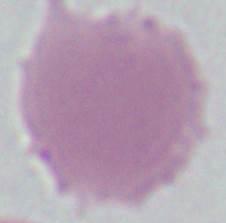
A red blood cell is seen. Photomicrograph. Captured at 1000x magnification.